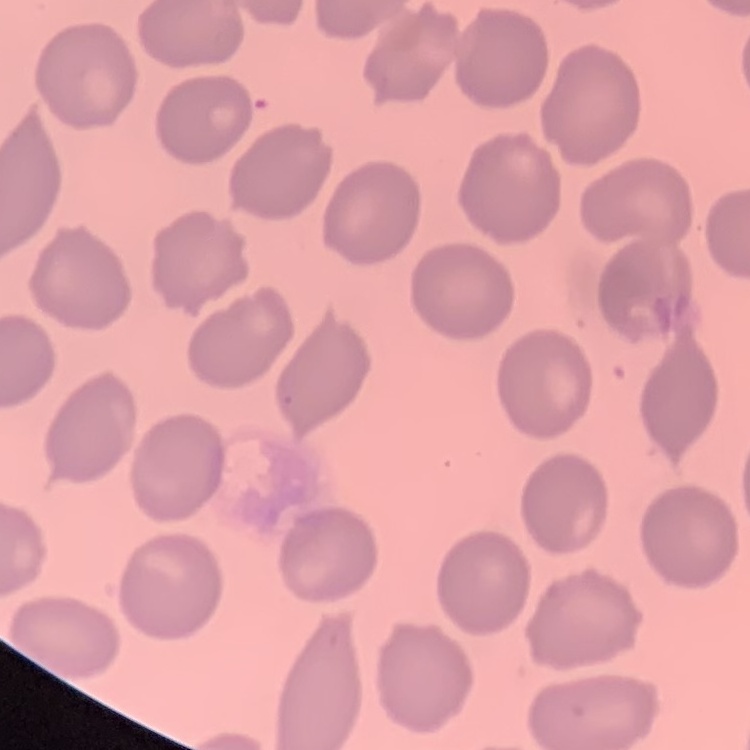
Summary:
  - Erythrocyte morphology: no rouleaux formation
  - Image type: one tile cut from a larger photomicrograph
  - Preparation: thin blood film
  - Stain: Field's or Giemsa